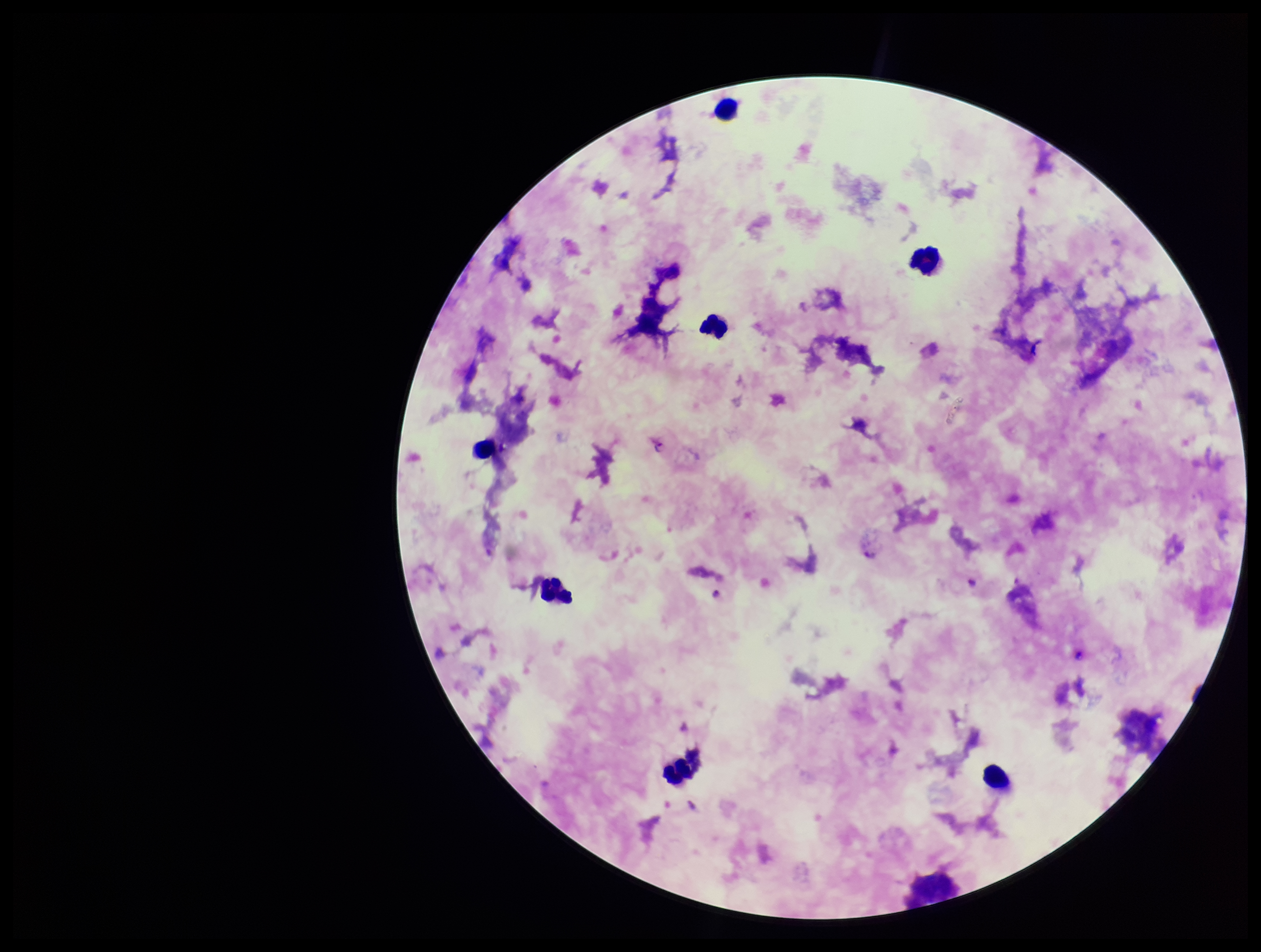
preparation = thick
image size = 1261×952 pixels
leukocyte count = 8
field of view = one from this slide
patient malaria status = infected
capture = smartphone photograph through the microscope eyepiece
species reported for this patient = Plasmodium falciparum
parasite count = 1
stain = Giemsa
Plasmodium parasites = identified